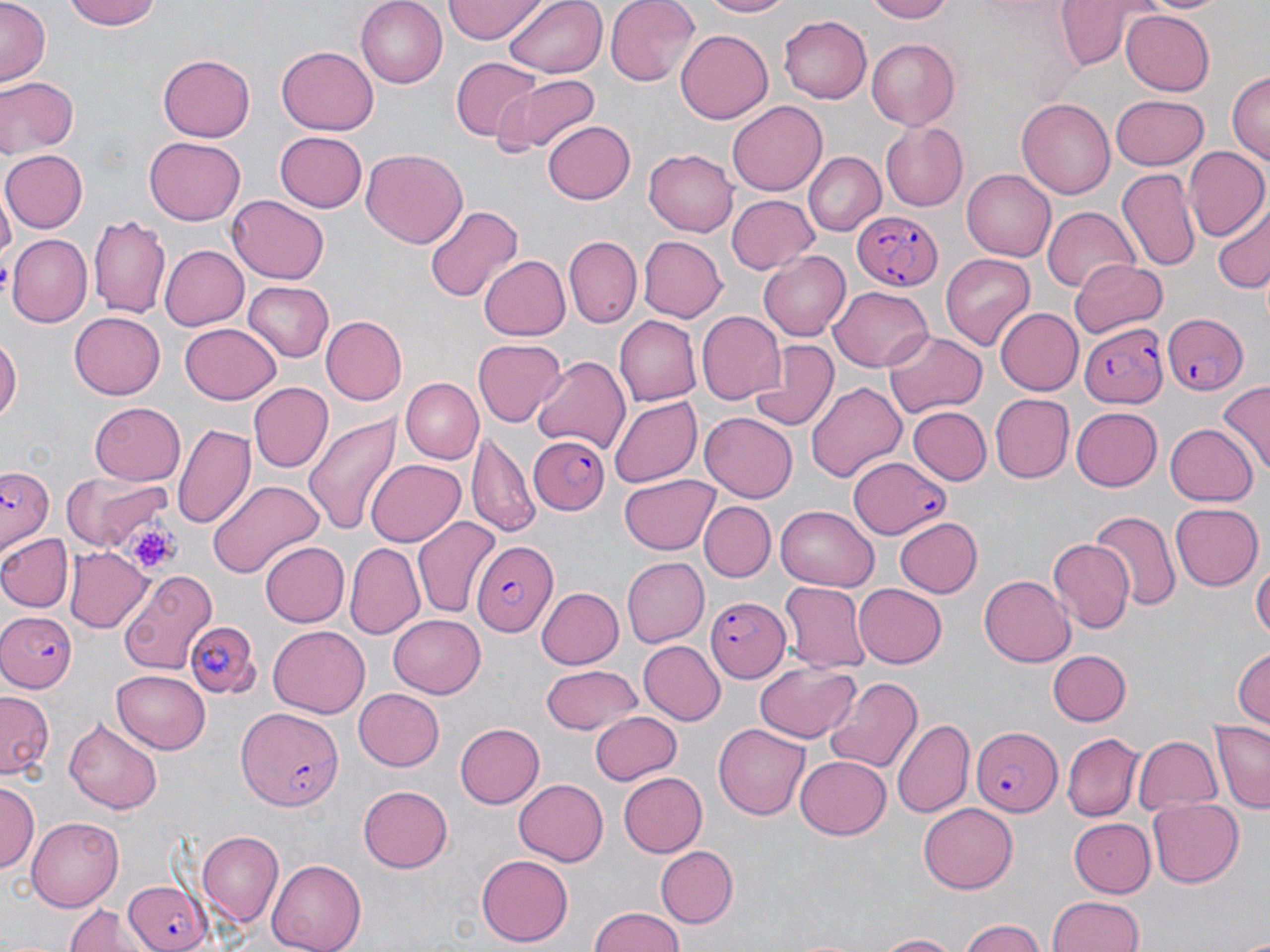

slide_level_diagnosis: Plasmodium falciparum
magnification: 1000x
image_size: 1270×952 pixels
stain: May-Grünwald-Giemsa
preparation: thin blood smear
platelet_locations: 'approximate bounding boxes as (x1,y1)-(x2,y2) corner pairs in pixels: (123,520)-(183,572)'
field_of_view: single
modality: optical microscopy
uninfected_red_blood_cell_locations_subset: 'approximate bounding boxes as (x1,y1)-(x2,y2) corner pairs in pixels: (68,0)-(163,30), (356,0)-(448,87), (445,0)-(544,42), (505,0)-(608,77), (605,0)-(700,87), (698,0)-(791,19), (865,0)-(957,23), (1051,0)-(1155,70), (1141,0)-(1229,16), (0,1)-(49,86), (1121,8)-(1215,94), (778,15)-(871,103), (675,29)-(772,124), (865,38)-(960,129), (276,45)-(376,135), (158,55)-(255,142), (450,58)-(545,144), (1228,72)-(1269,169), (492,73)-(601,157), (0,75)-(78,158), (1110,95)-(1209,170), (1017,97)-(1117,200), (728,99)-(829,196), (543,121)-(636,204), (881,122)-(970,210), (274,131)-(367,213), (146,135)-(246,223), (643,147)-(738,237), (360,148)-(468,249), (1184,149)-(1269,243), (3,150)-(87,234), (805,150)-(885,236), (1116,168)-(1199,274), (962,169)-(1056,260), (726,195)-(819,275), (225,197)-(329,284), (422,203)-(523,305), (1211,205)-(1270,296), (1041,206)-(1139,295), (89,214)-(169,317), (10,234)-(92,327), (635,235)-(727,323), (565,237)-(641,327), (161,245)-(249,330), (758,251)-(850,340), (939,252)-(1035,351), (480,255)-(571,342), (1070,259)-(1167,339), (245,282)-(334,361), (829,286)-(932,371), (995,307)-(1083,395), (696,311)-(785,406), (69,314)-(165,398), (614,315)-(701,406), (320,316)-(407,405), (181,321)-(281,402), (883,328)-(987,420), (0,333)-(21,428), (474,339)-(566,427), (749,339)-(840,430), (532,354)-(629,457), (398,376)-(482,465), (805,380)-(907,484), (1218,381)-(1270,469), (249,382)-(332,471), (991,393)-(1074,483), (609,395)-(703,487), (90,401)-(186,484), (907,406)-(990,486), (1072,407)-(1162,490), (302,412)-(403,535), (700,414)-(798,501), (172,421)-(256,531), (1166,425)-(1255,505), (467,429)-(540,542), (366,458)-(465,547), (63,472)-(168,554), (619,473)-(720,555), (206,479)-(322,582), (699,501)-(776,582), (1169,502)-(1262,591), (776,505)-(878,592), (1088,509)-(1181,613), (413,517)-(500,621), (895,518)-(984,598), (0,532)-(72,612), (1047,538)-(1134,632), (260,542)-(348,626), (346,543)-(424,637), (66,547)-(149,634), (1253,554)-(1269,650), (622,558)-(709,647), (118,569)-(217,675), (978,574)-(1074,667), (853,582)-(946,666), (778,583)-(870,672), (534,587)-(623,670), (389,613)-(487,696), (269,624)-(369,719), (638,642)-(723,724), (1230,643)-(1270,727), (1050,649)-(1131,727), (755,662)-(861,743), (541,664)-(645,735), (112,670)-(210,753), (825,675)-(924,775), (354,689)-(445,771), (0,691)-(54,780), (589,711)-(682,785), (893,718)-(972,816), (64,719)-(163,815), (1210,722)-(1270,814), (455,723)-(545,807), (713,723)-(810,819), (1062,731)-(1142,819), (1133,734)-(1222,816), (794,757)-(891,840), (616,772)-(707,856), (513,778)-(609,866), (0,781)-(38,877), (358,785)-(453,872), (1148,798)-(1244,887), (920,801)-(1019,893), (27,816)-(123,908), (1069,817)-(1155,897), (197,832)-(283,926), (657,846)-(739,927), (477,853)-(573,945), (265,858)-(367,952), (1046,895)-(1146,952), (63,905)-(147,952), (588,908)-(689,952), (959,920)-(1048,952), (869,933)-(964,951)'
plasmodium_falciparum_infected_red_blood_cell_locations_subset: 'approximate bounding boxes as (x1,y1)-(x2,y2) corner pairs in pixels: (854,207)-(944,294), (1161,312)-(1246,395), (1078,322)-(1164,407), (528,433)-(611,514), (849,456)-(948,537), (3,464)-(58,550), (472,540)-(561,634), (708,595)-(791,681), (0,610)-(79,695), (186,619)-(261,702), (239,708)-(343,809), (972,724)-(1063,816)'